Assess this cell for malaria.
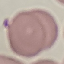
It is uninfected.

Automatically extracted cell patch, resized to 64 × 64 pixels. Acquired by smartphone through the microscope eyepiece. Thin blood film. Giemsa-stained preparation.